Assess this cell for malaria.
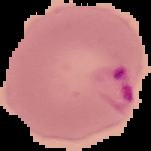
Parasitized.

Summary:
  - Image size: 151×151 pixels
  - Preparation: thin blood smear
  - Image type: segmented cell region with the area outside set to black